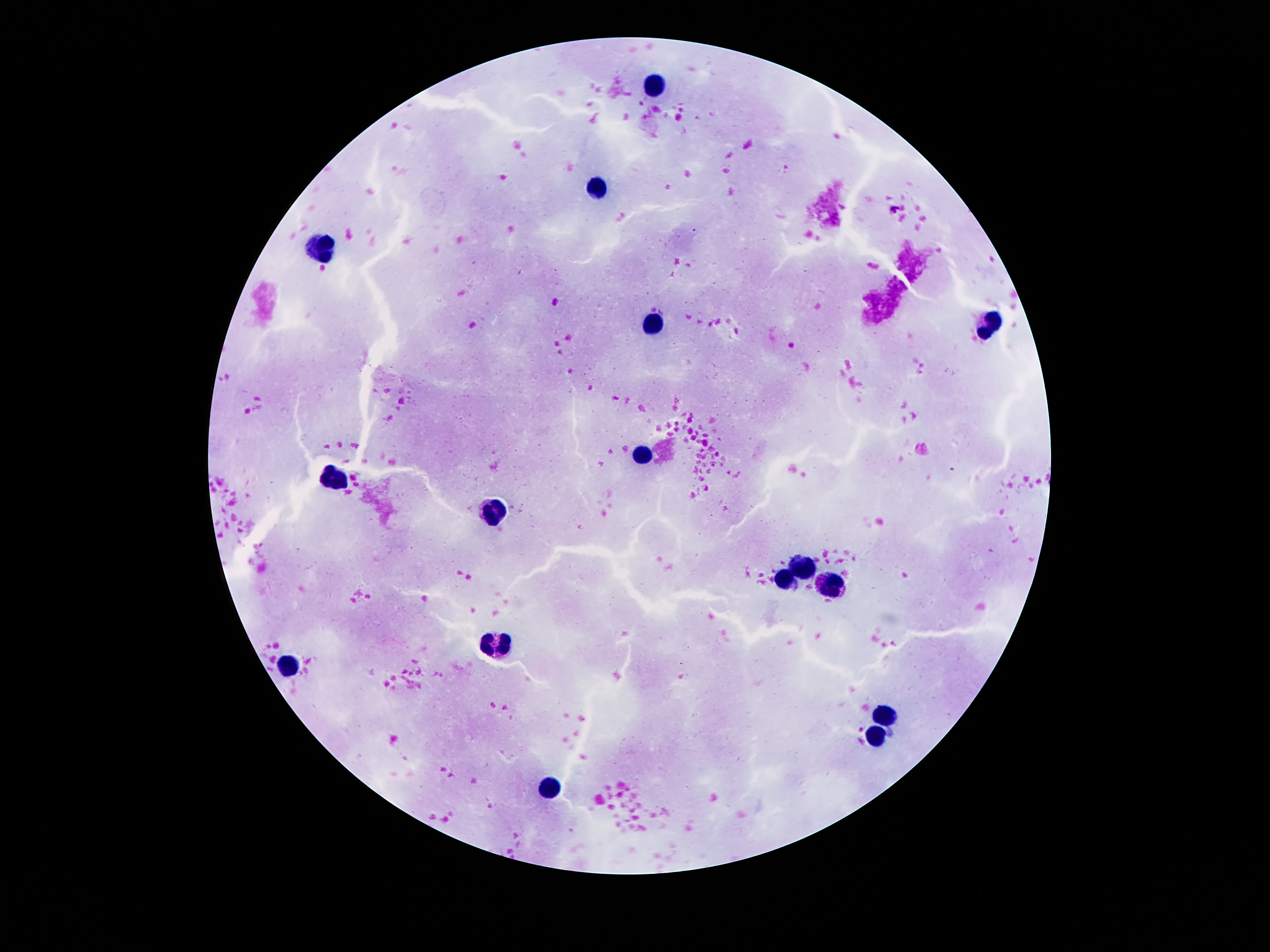

Approximate object centers, in pixels from the top-left corner.
Summary:
  - Leukocyte locations: (x=656, y=86), (x=597, y=188), (x=318, y=247), (x=652, y=323), (x=986, y=326), (x=642, y=453), (x=335, y=478), (x=491, y=514), (x=803, y=568), (x=782, y=578), (x=830, y=584), (x=493, y=646), (x=291, y=665), (x=879, y=716), (x=873, y=739), (x=549, y=785)
  - Field of view: single
  - Patient malaria status: uninfected
  - Preparation: thick blood film
  - Magnification: 100x
  - Image size: 1270×952 pixels
  - Capture: smartphone camera through the microscope eyepiece
  - Stain: Giemsa